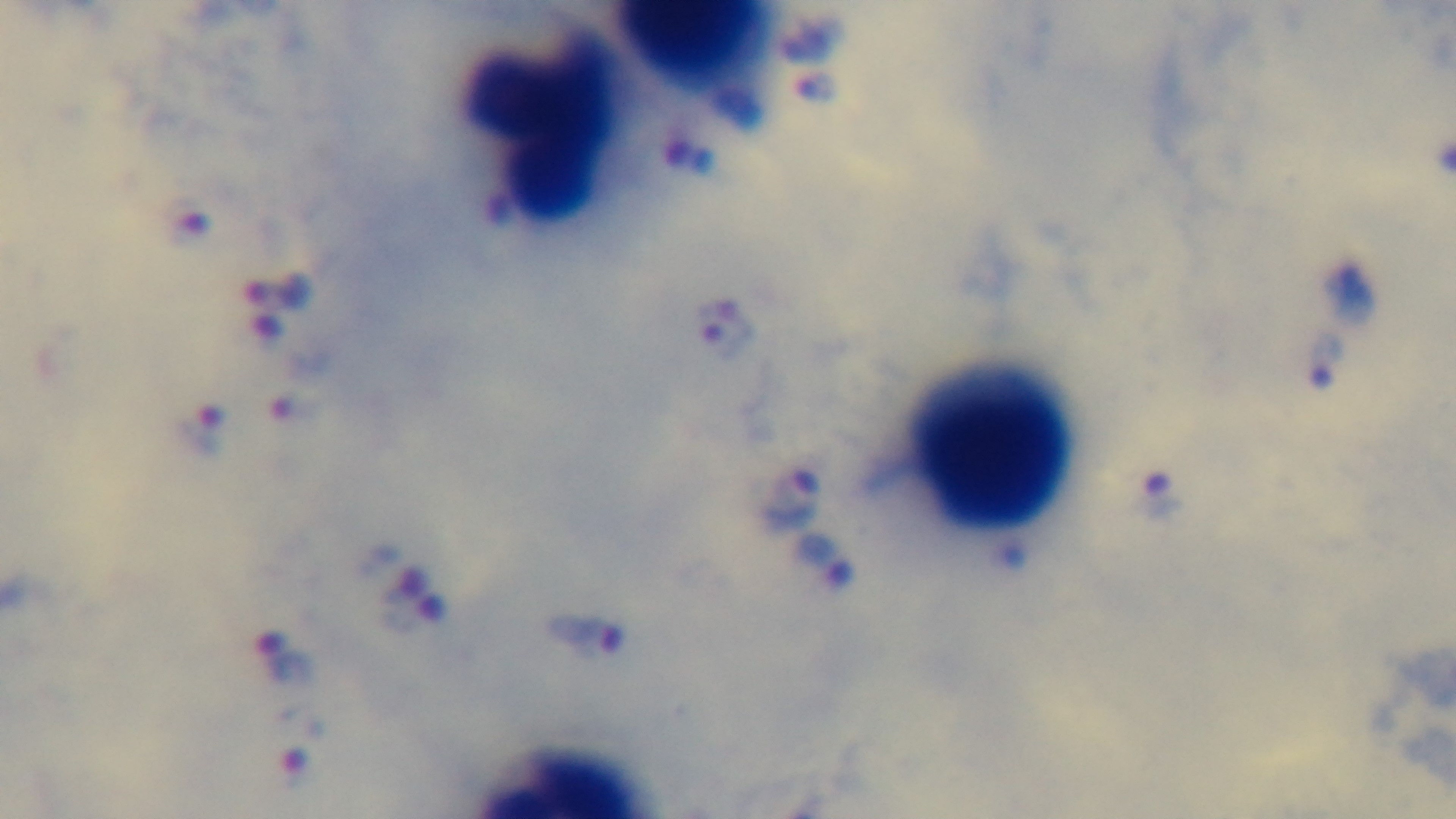

Summary:
  - Capture: mounted 4K digital camera
  - Objective: 100x oil immersion
  - Preparation: thick
  - Modality: light microscopy
  - Stain: Giemsa
  - Field of view: one from the slide
  - Malaria status: infected